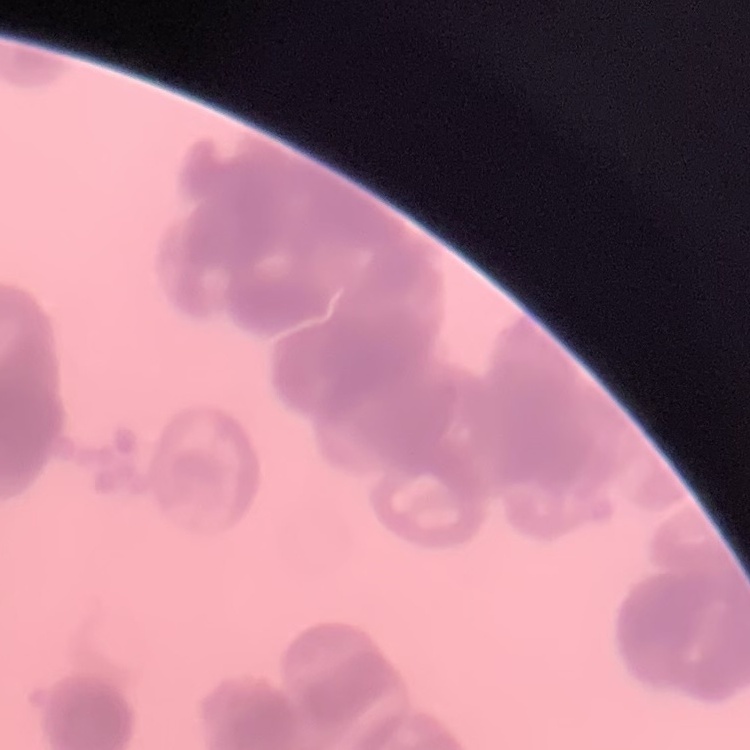
Summary:
  - Erythrocyte morphology: rouleaux formation
  - Image type: square crop of a larger photomicrograph
  - Preparation: thin blood smear
  - Stain: Field's or Giemsa